Report the malaria status of this cell.
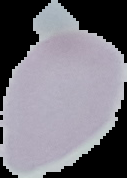

Uninfected.

Image is 127×178 pixels. From a thin blood film. Segmented cell region on a black background.